Assess the morphology of the red blood cells.
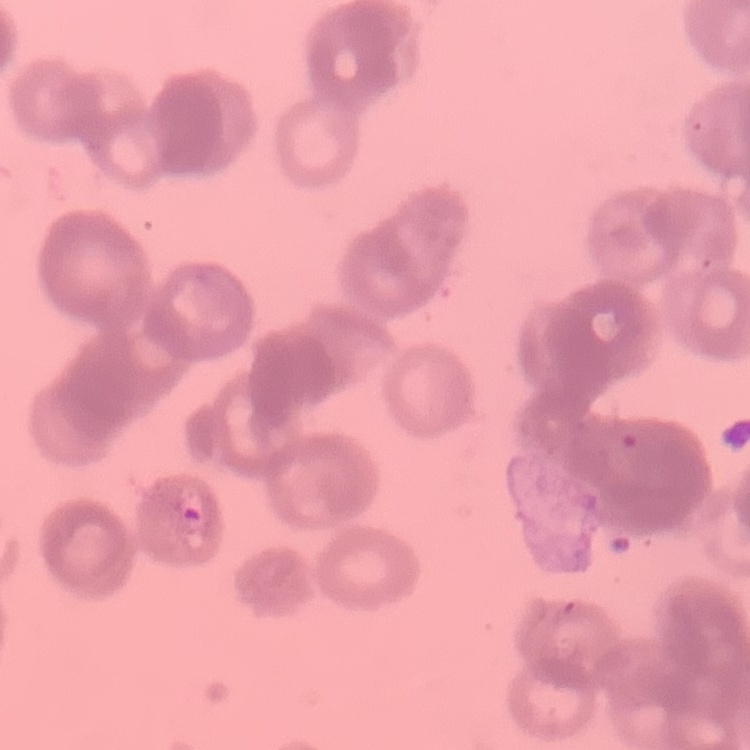
They show rouleaux formation.

Summary:
  - Preparation: thin peripheral smear
  - Stain: Field's or Giemsa
  - Image type: one tile cut from a larger photomicrograph